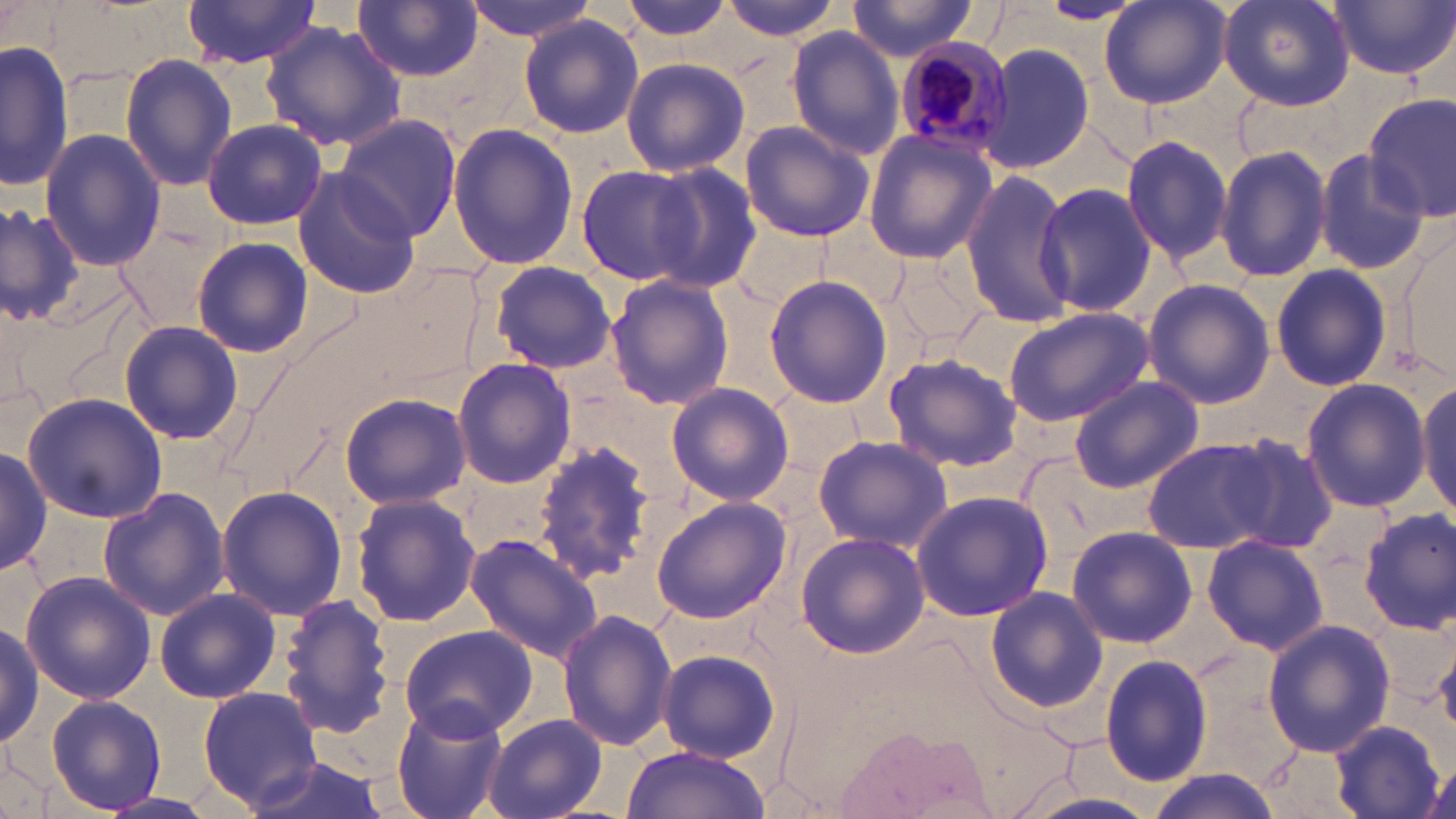
Summary:
  - Coordinate format: approximate bounding boxes as (x1,y1)-(x2,y2) corner pairs in pixels
  - Plasmodium malariae-infected red blood cell locations: (891,37)-(1016,163)
  - Uninfected red blood cell locations: (462,0)-(601,41), (614,0)-(738,45), (715,0)-(847,42), (1099,0)-(1232,110), (1218,0)-(1355,110), (1330,0)-(1455,80), (178,1)-(324,70), (845,1)-(986,63), (1036,1)-(1145,24), (354,2)-(482,81), (519,15)-(645,138), (262,21)-(408,151), (784,27)-(906,159), (0,39)-(72,195), (981,44)-(1094,174), (119,54)-(237,192), (619,57)-(750,176), (1365,94)-(1455,219), (334,112)-(461,240), (201,118)-(328,230), (737,120)-(876,243), (448,123)-(578,271), (862,129)-(996,264), (39,130)-(165,271), (1120,132)-(1234,265), (1215,143)-(1332,285), (1313,146)-(1431,276), (644,160)-(762,293), (575,165)-(701,285), (293,169)-(419,300), (960,170)-(1078,327), (1034,182)-(1159,316), (0,200)-(83,327), (117,222)-(229,332), (1401,234)-(1455,379), (190,236)-(313,358), (888,246)-(991,349), (491,260)-(618,373), (1269,263)-(1393,392), (366,264)-(482,390), (764,275)-(892,410), (606,276)-(735,412), (1142,279)-(1275,408), (1002,305)-(1154,425), (118,319)-(245,446), (880,351)-(1023,472), (451,357)-(577,489), (1068,376)-(1203,491), (1301,379)-(1431,512), (1416,381)-(1455,523), (666,382)-(794,507), (767,384)-(864,481), (22,392)-(165,523), (339,392)-(472,509), (1220,432)-(1341,554), (811,433)-(953,552), (1140,437)-(1285,553), (532,442)-(656,586), (0,443)-(50,578), (97,486)-(230,622), (216,486)-(346,621), (910,489)-(1056,622), (349,494)-(481,628), (650,496)-(793,625), (1358,508)-(1455,635), (1066,525)-(1198,648), (795,532)-(930,659), (463,534)-(602,663), (1203,534)-(1329,655), (20,571)-(154,703), (984,586)-(1107,713), (153,588)-(282,703), (278,595)-(396,738), (557,607)-(677,752), (0,619)-(42,749), (1260,619)-(1395,759), (397,624)-(539,740), (1436,638)-(1456,736), (657,648)-(782,764), (1099,654)-(1213,786), (197,684)-(327,812), (46,694)-(166,813), (390,701)-(510,819), (482,715)-(608,819), (1331,720)-(1449,818), (620,747)-(772,819), (240,753)-(392,819), (1143,772)-(1282,819), (1014,790)-(1161,819), (100,791)-(218,818)
  - Slide-level diagnosis: Plasmodium malariae
  - Modality: optical microscopy
  - Preparation: thin blood smear
  - Stain: May-Grünwald-Giemsa
  - Field of view: single
  - Magnification: 1000x
  - Image size: 1456×819 pixels